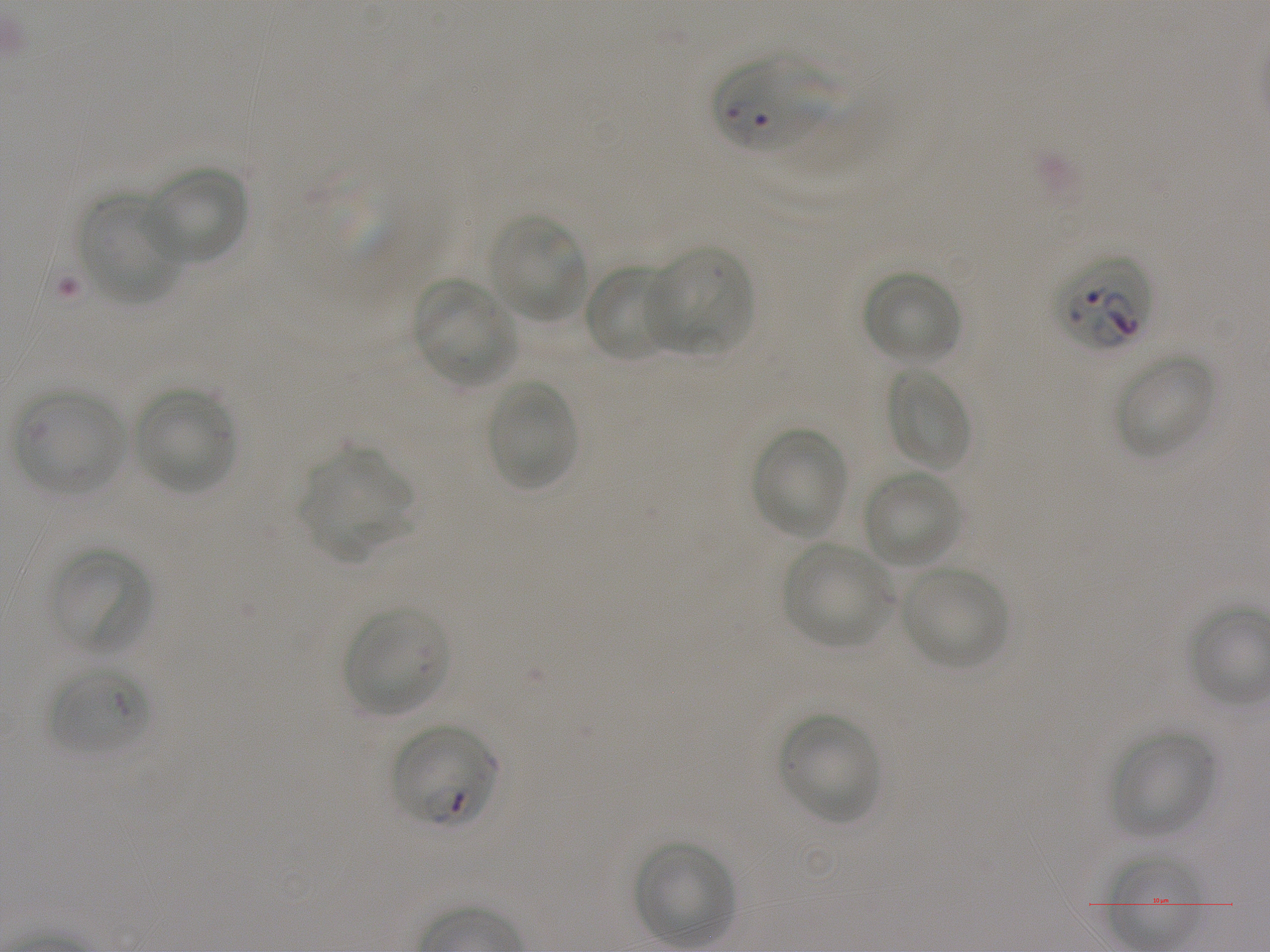

Approximate bounding boxes as [x1, y1, x2, y2] in pixels. Not every red blood cell is marked. A life-cycle stage — or a range of stages, where the recorded stages span more than one — follows each staged infected red blood cell.
Summary:
  - Locations of infected red blood cells: [714, 56, 837, 152]; [1056, 252, 1152, 353]; [389, 723, 500, 830] ring
  - Locations of red blood cells of indeterminate infection status: [48, 664, 149, 757]
  - Locations of uninfected red blood cells: [144, 165, 250, 266], [78, 193, 184, 306], [485, 214, 588, 323], [645, 244, 754, 355], [582, 263, 678, 363], [862, 269, 961, 366], [413, 278, 518, 387], [1117, 354, 1215, 458], [886, 366, 973, 473], [485, 380, 578, 491], [135, 387, 236, 495], [14, 388, 126, 496], [750, 426, 849, 539], [303, 450, 413, 557], [864, 470, 963, 570], [782, 543, 893, 650], [49, 546, 153, 655], [901, 566, 1007, 669], [341, 604, 451, 716], [779, 714, 881, 824], [1110, 728, 1216, 837], [635, 840, 736, 946], [1104, 853, 1208, 944]
  - Objective: 100x, oil immersion, numerical aperture 1.25
  - Donor blood group: A+
  - Stain: Giemsa
  - Field of view: one from this slide
  - Image size: 1270×952 pixels
  - Preparation: thin blood smear
  - Culture: static in-vitro P. falciparum strain NF54